Locate malaria parasites and leukocytes.
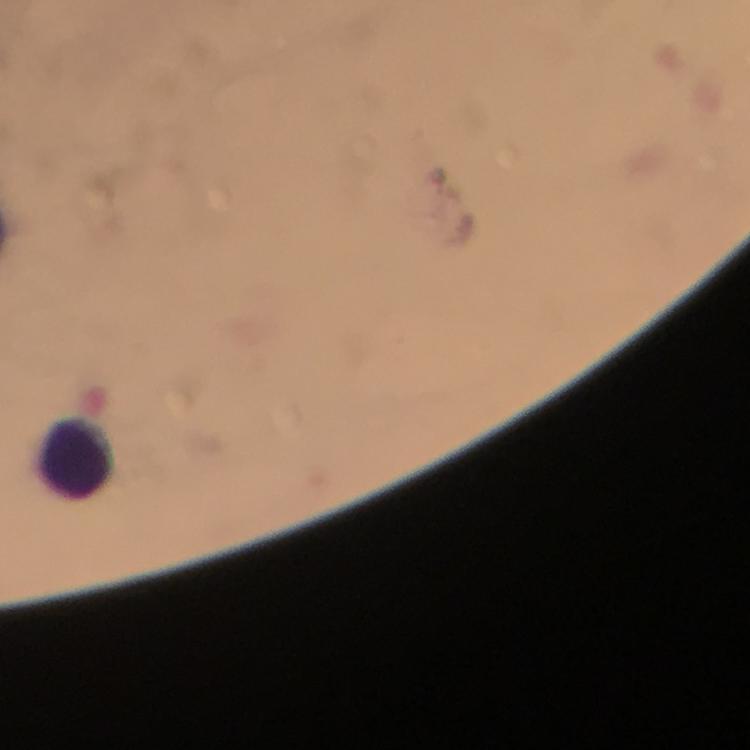
No malaria parasites detected.
Approximate centers as (x, y) in pixels.
Leukocytes: (77, 458).

Immersion oil was used. From a diagnostic examination for malaria. Photographed through the microscope with a smartphone camera. A crop from one field of view. Image is 750×750 pixels. Thick blood film. 100x magnification. Giemsa-stained preparation.